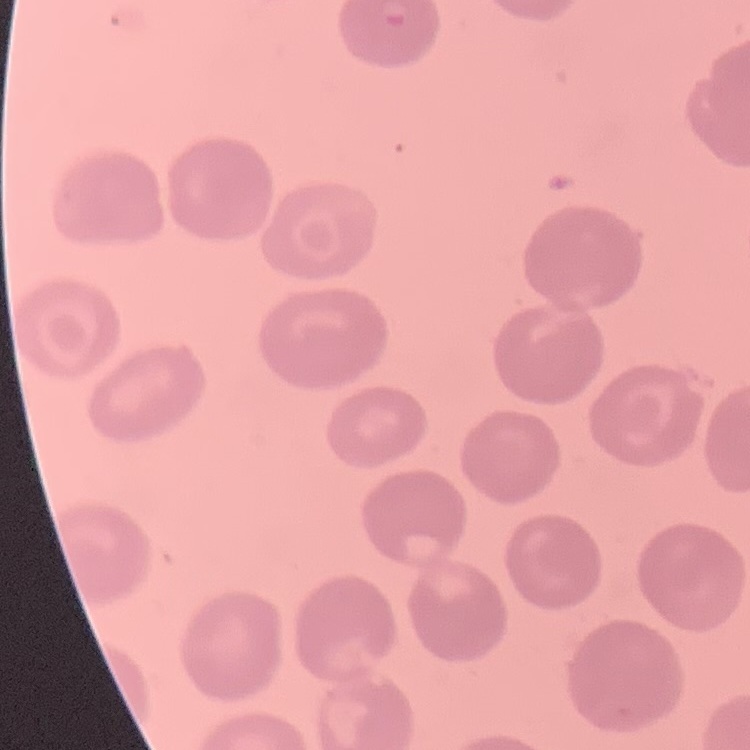
Summary:
  - Erythrocyte morphology: no rouleaux formation
  - Image type: one tile cut from a larger photomicrograph
  - Preparation: thin blood film
  - Stain: Field's or Giemsa